State which parasite is depicted.
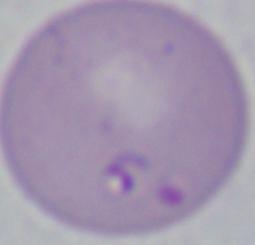

This is Babesia.

Summary:
  - Magnification: 1000x
  - Modality: micrograph